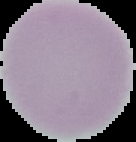

Summary:
  - Preparation: thin blood smear
  - Image type: segmented cell region on a black background
  - Malaria status: uninfected
  - Image size: 136×142 pixels